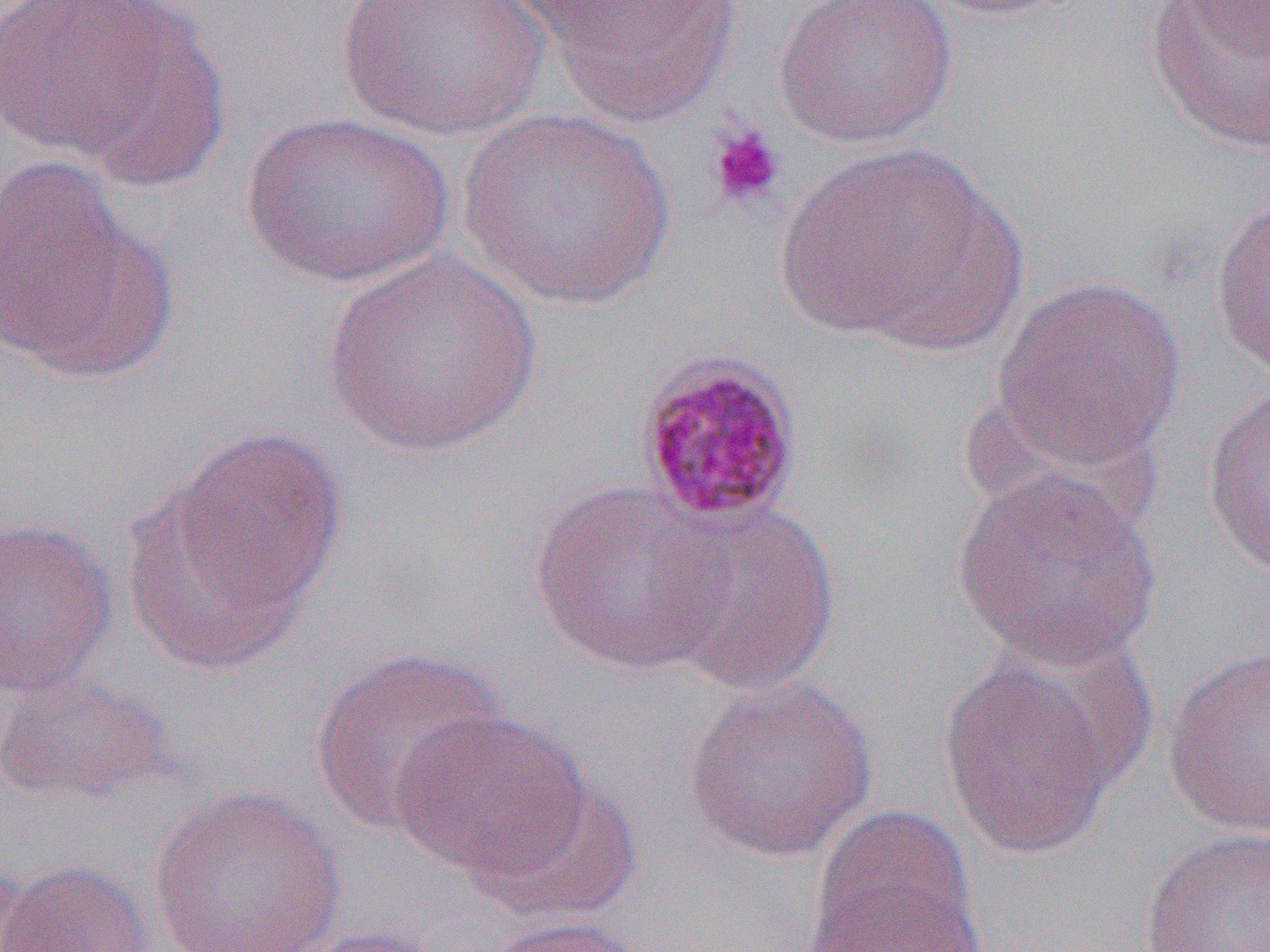
Summary:
  - Coordinate format: approximate bounding boxes as (x1,y1)-(x2,y2) corner pairs in pixels
  - Uninfected red blood cell locations: (336,0)-(548,142), (522,0)-(745,127), (774,0)-(958,148), (908,0)-(1082,20), (1143,0)-(1270,157), (1178,0)-(1270,60), (0,1)-(222,175), (456,108)-(676,310), (239,111)-(454,290), (772,141)-(1022,353), (0,155)-(171,384), (1208,191)-(1270,382), (321,249)-(545,459), (991,274)-(1187,472), (1200,383)-(1270,583), (153,426)-(347,634), (951,466)-(1162,670), (528,481)-(733,675), (656,499)-(842,696), (0,518)-(117,698), (1161,643)-(1270,837), (308,645)-(508,835), (936,646)-(1135,862), (1,671)-(173,806), (682,674)-(879,865), (389,709)-(592,881), (472,777)-(642,924), (145,783)-(350,952), (805,805)-(984,949), (1139,825)-(1270,952), (1,859)-(154,952), (806,882)-(990,952), (476,915)-(648,952), (280,924)-(457,952)
  - Platelet locations: (707,124)-(784,208)
  - Plasmodium malariae-infected red blood cell locations: (634,350)-(805,529)
  - Slide-level diagnosis: Plasmodium malariae
  - Image size: 1270×952 pixels
  - Modality: light microscopy
  - Magnification: 1000x
  - Field of view: one of a larger specimen
  - Preparation: thin blood smear